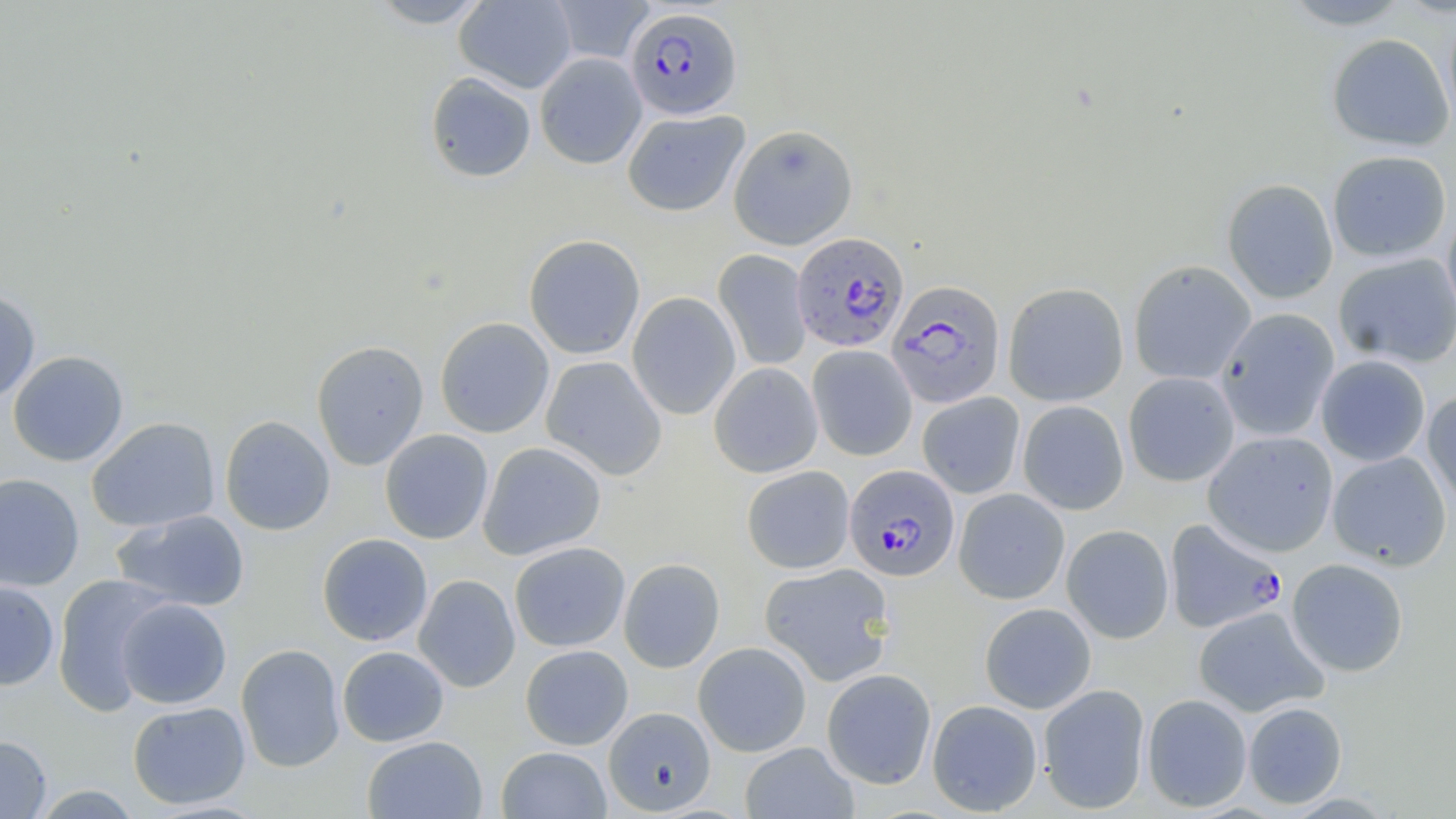 Approximate bounding boxes as [x1, y1, x2, y2] in pixels. Plasmodium falciparum-infected red blood cell locations: [625, 6, 742, 119], [790, 232, 909, 352], [886, 280, 1005, 408], [844, 464, 960, 581], [1164, 518, 1288, 633]. Uninfected red blood cell locations: [366, 0, 494, 28], [454, 0, 577, 93], [549, 0, 655, 65], [1278, 0, 1415, 30], [1443, 8, 1456, 133], [1327, 33, 1454, 151], [535, 52, 647, 169], [424, 72, 536, 183], [622, 109, 749, 216], [728, 123, 858, 250], [1326, 150, 1452, 263], [1221, 178, 1339, 304], [1441, 209, 1456, 325], [523, 234, 646, 360], [714, 249, 812, 370], [1333, 253, 1456, 369], [1128, 259, 1256, 385], [1003, 282, 1129, 407], [0, 290, 41, 402], [627, 292, 741, 420], [1216, 308, 1339, 441], [434, 317, 554, 438], [312, 339, 429, 470], [807, 344, 917, 461], [8, 350, 129, 466], [1316, 354, 1431, 466], [540, 356, 668, 480], [709, 362, 823, 478], [1123, 372, 1240, 487], [1422, 389, 1456, 514], [916, 392, 1025, 498], [1017, 400, 1129, 515], [220, 415, 336, 535], [86, 416, 220, 533], [379, 429, 494, 544], [1202, 430, 1339, 557], [478, 442, 607, 560], [1327, 451, 1452, 571], [742, 466, 855, 574], [0, 472, 84, 591], [954, 488, 1070, 605], [111, 509, 250, 612], [1061, 524, 1174, 644], [317, 533, 432, 646], [509, 542, 630, 652], [618, 558, 725, 673], [1286, 558, 1409, 677], [759, 562, 896, 686], [51, 574, 174, 715], [413, 574, 520, 693], [0, 581, 60, 691], [116, 598, 231, 709], [979, 602, 1096, 713], [1193, 606, 1328, 717], [693, 642, 812, 757], [235, 644, 346, 772], [520, 644, 633, 750], [337, 646, 449, 747], [821, 668, 937, 789], [1038, 683, 1151, 814], [1141, 694, 1252, 812], [927, 699, 1043, 816], [127, 701, 251, 809], [1242, 701, 1347, 809], [603, 706, 716, 815], [0, 735, 52, 818], [362, 735, 488, 819], [740, 742, 858, 819], [496, 746, 611, 819], [30, 785, 143, 818]. Slide-level diagnosis: Plasmodium falciparum. Image is 1456×819 pixels. May-Grünwald-Giemsa stain. Optical microscopy. One field of a larger specimen. Captured at 1000x magnification. Thin blood smear.